Identify the parasite.
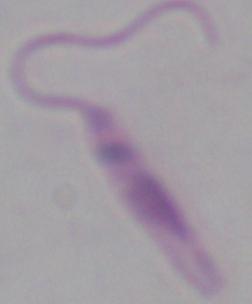

This is Leishmania.

Photomicrograph. 1000x magnification.